Assess this cell for malaria.
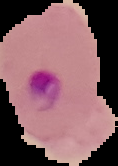

It is parasitized.

The area outside the segmented cell region is set to black. Image is 118×166 pixels. From a thin blood film.